Name the parasite shown.
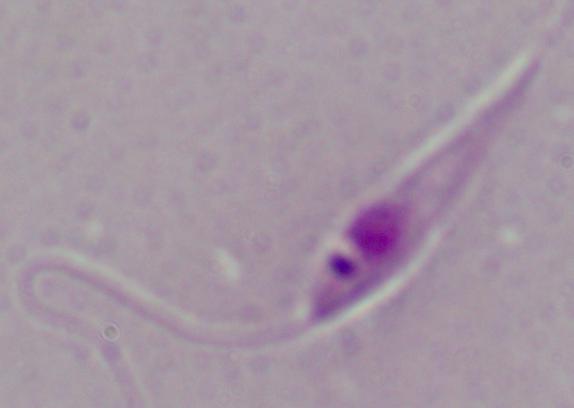

Leishmania.

1000x magnification. Photomicrograph.